Assess this cell for malaria.
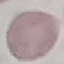

Uninfected.

{
  "image_type": "cell patch, automatically extracted from a larger field of view and resized to 64 × 64 pixels",
  "preparation": "thin smear",
  "capture": "smartphone through the microscope eyepiece",
  "stain": "Giemsa"
}